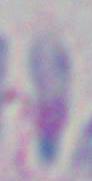

Summary:
  - Modality: micrograph
  - Magnification: 1000x
  - Identification: Toxoplasma gondii